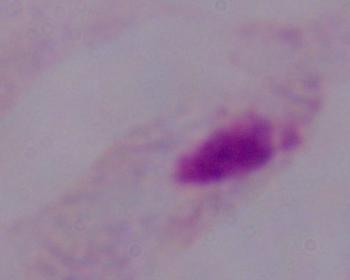

1000x magnification. Micrograph. A trichomonad is shown.